Outline each Babesia divergens-infected red blood cell.
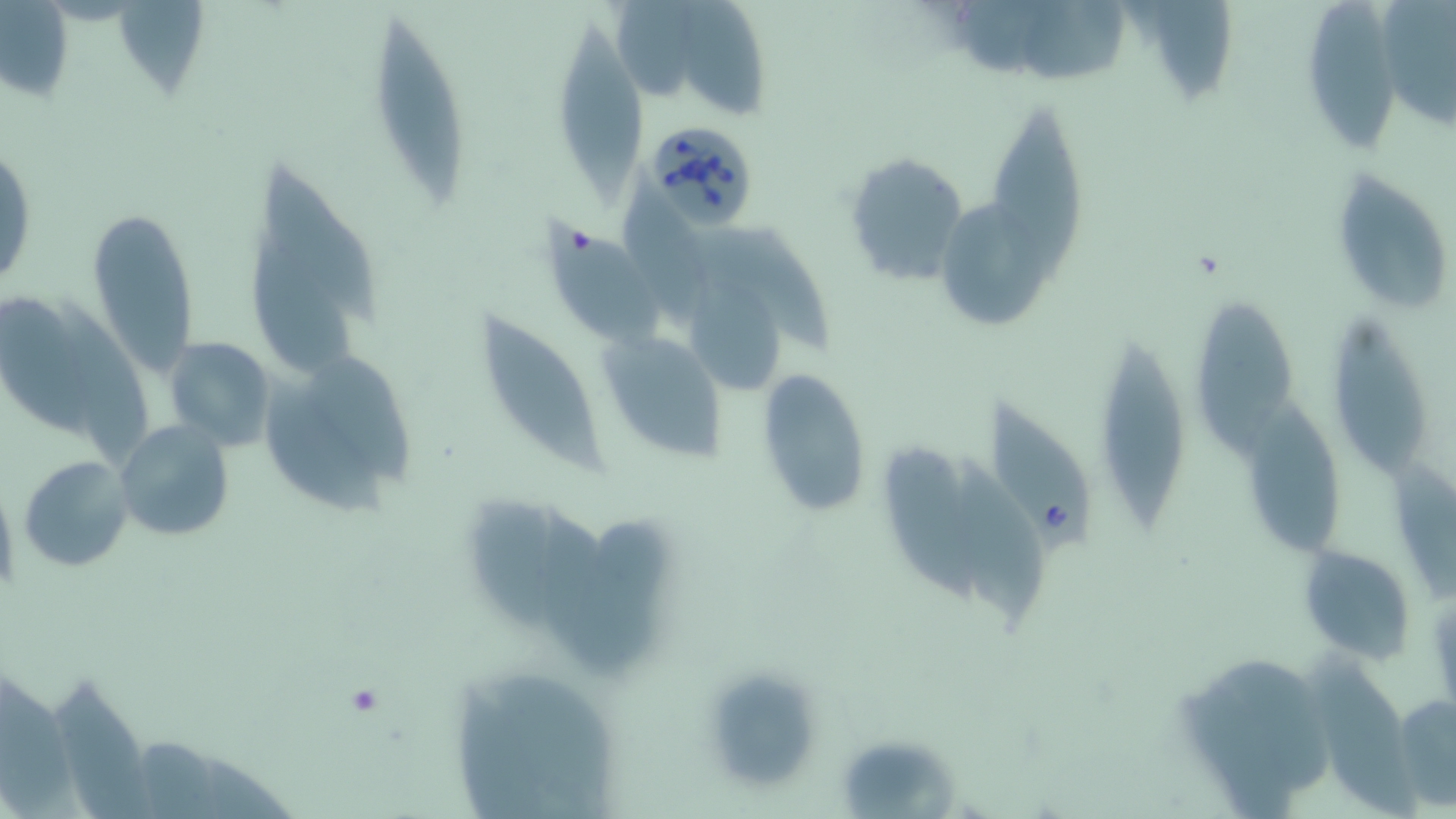
Approximate bounding boxes as (x1,y1)-(x2,y2) corner pairs in pixels.
Babesia divergens-infected red blood cells: (641,119)-(761,230).

slide_level_diagnosis: Babesia divergens
modality: light microscopy
stain: May-Grünwald-Giemsa
field_of_view: single
preparation: thin blood smear
uninfected_red_blood_cell_locations: 'approximate bounding boxes as (x1,y1)-(x2,y2) corner pairs in pixels: (618,0)-(696,104), (1381,0)-(1456,137), (1,2)-(76,107), (113,2)-(210,105), (682,2)-(771,118), (1306,2)-(1402,151), (1021,3)-(1129,88), (1135,3)-(1241,111), (370,16)-(472,208), (557,30)-(651,207), (987,104)-(1089,283), (1,140)-(36,294), (842,150)-(969,288), (619,163)-(709,324), (256,165)-(379,326), (1330,169)-(1456,314), (85,204)-(202,378), (547,223)-(664,349), (702,226)-(840,355), (241,231)-(360,380), (691,279)-(782,396), (1,299)-(97,431), (1200,301)-(1298,458), (67,305)-(158,465), (476,312)-(604,478), (1324,314)-(1427,477), (163,336)-(276,449), (1102,339)-(1191,533), (610,341)-(729,462), (314,355)-(415,480), (756,367)-(872,517), (257,382)-(387,518), (1248,398)-(1344,555), (987,403)-(1095,554), (115,419)-(234,543), (883,445)-(979,609), (953,453)-(1046,626), (19,454)-(134,573), (1299,545)-(1416,661), (1313,659)-(1434,819), (695,663)-(829,799), (0,667)-(80,819), (50,679)-(151,819), (457,683)-(554,819), (1394,691)-(1455,808), (845,742)-(961,819)'
magnification: 1000x
image_size: 1456×819 pixels